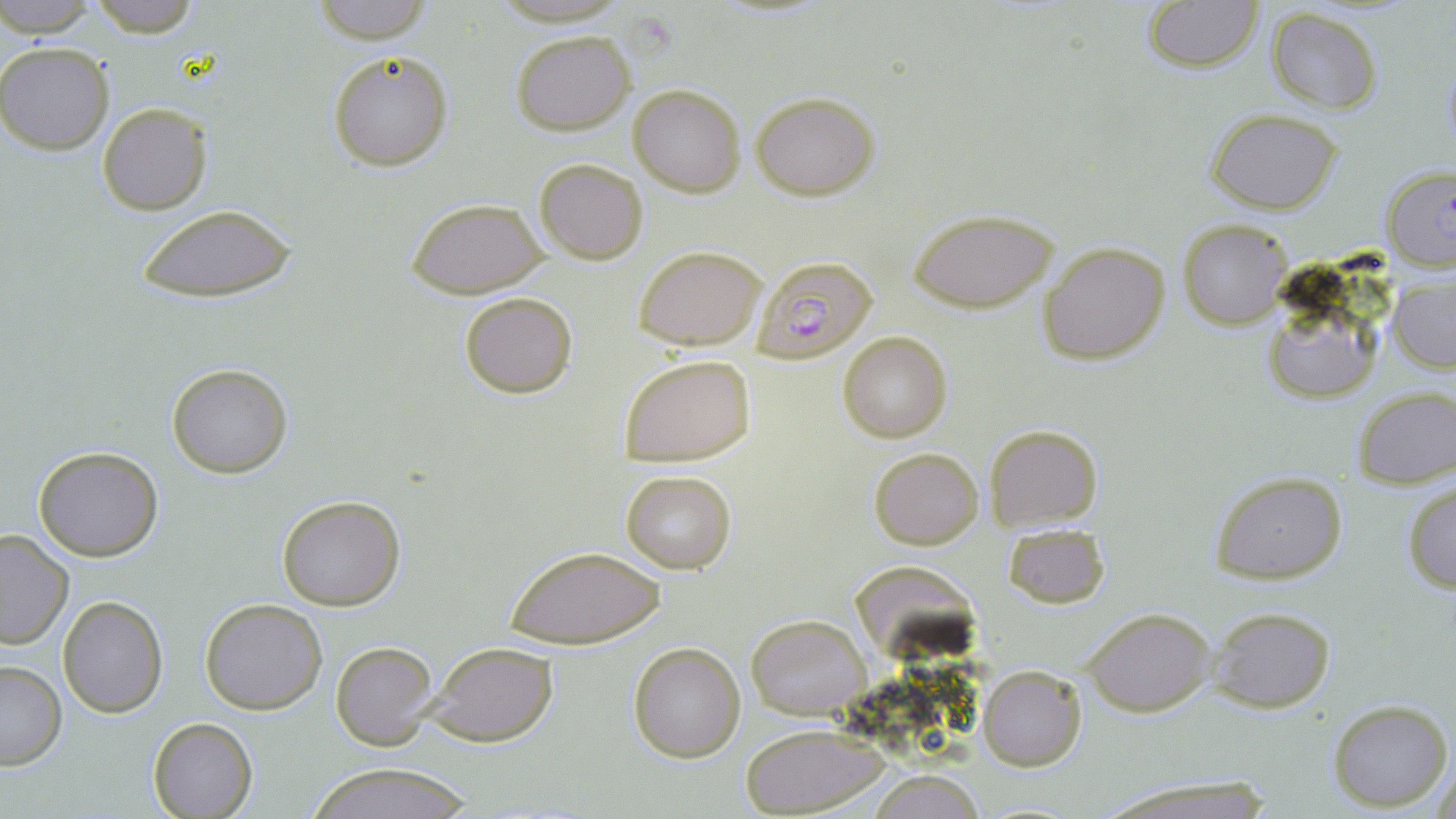

slide-level diagnosis = Plasmodium falciparum
field of view = single
image size = 1456×819 pixels
Plasmodium falciparum-infected red blood cell locations = approximate bounding boxes as [x1, y1, x2, y2] in pixels: [751, 252, 881, 363]
modality = optical microscopy
preparation = thin blood film
uninfected red blood cell locations = approximate bounding boxes as [x1, y1, x2, y2] in pixels: [85, 0, 202, 39], [0, 1, 105, 36], [308, 1, 435, 44], [1140, 1, 1263, 73], [1265, 8, 1384, 115], [510, 29, 634, 134], [0, 42, 116, 156], [326, 50, 454, 172], [628, 83, 746, 198], [751, 92, 879, 201], [97, 102, 213, 217], [1208, 108, 1343, 213], [533, 157, 648, 264], [1380, 164, 1456, 271], [406, 197, 547, 298], [133, 203, 299, 304], [907, 207, 1060, 312], [1178, 218, 1293, 330], [1038, 240, 1171, 367], [633, 245, 767, 348], [1257, 275, 1391, 409], [1388, 275, 1455, 374], [458, 289, 579, 399], [838, 330, 953, 444], [617, 353, 758, 466], [165, 361, 294, 479], [1350, 386, 1456, 489], [985, 423, 1102, 533], [32, 445, 164, 562], [869, 447, 983, 550], [620, 470, 738, 574], [1207, 470, 1350, 586], [1402, 481, 1455, 594], [276, 494, 406, 610], [1003, 523, 1112, 608], [0, 527, 74, 652], [505, 543, 668, 649], [58, 596, 169, 718], [200, 598, 327, 715], [1082, 606, 1216, 715], [1208, 606, 1335, 713], [745, 614, 871, 719], [332, 641, 439, 750], [627, 641, 746, 764], [425, 642, 560, 748], [0, 660, 67, 771], [978, 664, 1087, 770], [1326, 698, 1453, 810], [148, 717, 259, 818], [738, 724, 887, 817], [1430, 749, 1455, 818], [303, 766, 480, 819], [865, 771, 990, 818], [1093, 776, 1275, 819]
magnification = 1000x
stain = May-Grünwald-Giemsa